State which parasite is depicted.
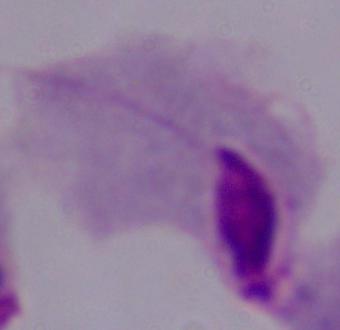

A trichomonad.

magnification = 1000x
modality = micrograph